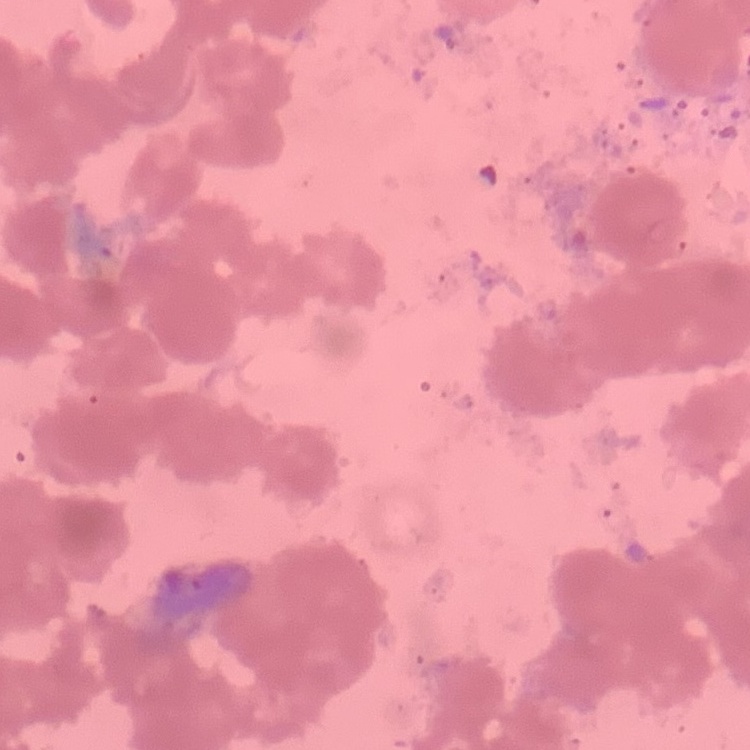
Summary:
  - Red blood cell morphology: rouleaux formation
  - Preparation: thin peripheral smear
  - Stain: Field's or Giemsa
  - Image type: one tile cut from a larger photomicrograph